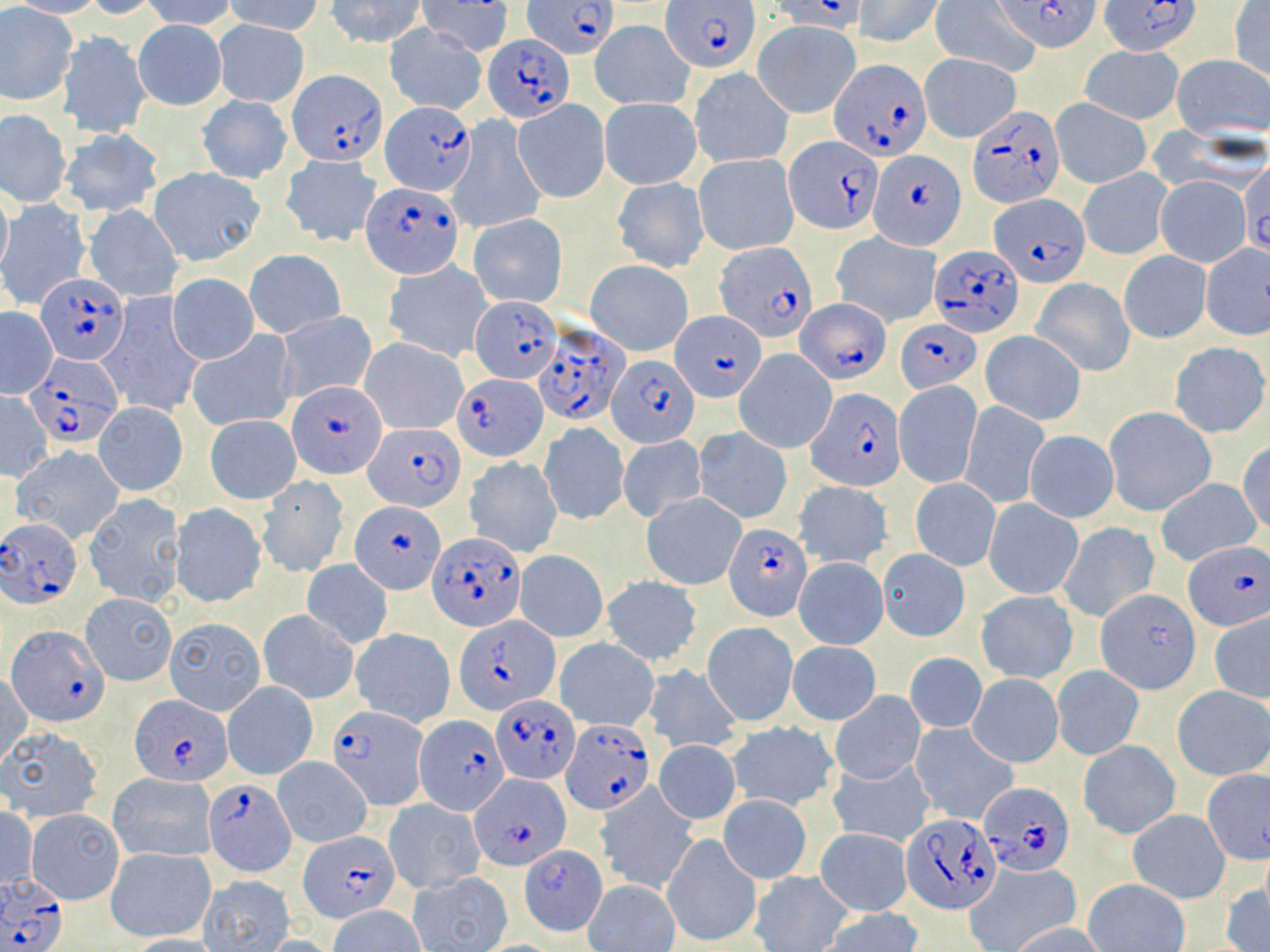 Approximate bounding boxes as (x1,y1)-(x2,y2) corner pairs in pixels. Plasmodium falciparum-infected red blood cell locations: (524,0)-(618,60), (663,0)-(758,72), (774,0)-(867,31), (994,1)-(1102,54), (1100,1)-(1204,55), (483,34)-(573,123), (831,57)-(933,169), (288,70)-(385,167), (379,101)-(475,193), (966,105)-(1065,208), (783,134)-(885,235), (869,150)-(964,251), (362,182)-(463,276), (990,196)-(1088,282), (715,241)-(817,340), (929,245)-(1023,337), (36,273)-(128,363), (469,296)-(565,385), (795,297)-(889,384), (673,312)-(763,401), (897,321)-(979,395), (534,322)-(629,428), (607,353)-(697,448), (26,355)-(122,445), (457,376)-(547,463), (288,379)-(386,477), (808,387)-(905,491), (365,422)-(465,511), (352,500)-(443,593), (1,517)-(83,609), (725,523)-(812,621), (427,532)-(527,631), (1183,540)-(1270,631), (1096,590)-(1199,693), (455,616)-(561,713), (7,625)-(108,725), (494,693)-(576,781), (131,696)-(230,786), (326,703)-(430,809), (414,714)-(509,815), (561,718)-(653,815), (471,774)-(570,870), (203,779)-(297,876), (980,781)-(1073,875), (900,814)-(1002,914), (299,830)-(399,924), (522,845)-(606,933), (0,873)-(69,952). Uninfected red blood cell locations: (7,0)-(107,18), (81,0)-(165,19), (141,0)-(239,31), (226,0)-(326,36), (325,0)-(426,48), (853,0)-(943,48), (927,0)-(1040,77), (419,1)-(513,54), (1229,3)-(1270,82), (0,6)-(78,107), (588,19)-(694,110), (753,19)-(861,118), (133,20)-(227,109), (213,20)-(309,107), (384,23)-(488,114), (58,32)-(149,138), (1079,45)-(1184,124), (919,53)-(1020,142), (1173,54)-(1270,139), (689,67)-(792,168), (197,95)-(293,184), (599,98)-(702,189), (1050,98)-(1152,189), (513,99)-(610,203), (0,112)-(71,206), (448,120)-(547,234), (61,132)-(163,217), (694,153)-(799,256), (280,155)-(383,247), (1239,164)-(1270,257), (150,167)-(265,264), (1078,167)-(1172,259), (1154,175)-(1251,267), (611,176)-(708,271), (0,187)-(13,282), (1,199)-(90,310), (86,204)-(184,301), (467,213)-(569,308), (829,232)-(941,328), (1201,244)-(1270,341), (245,249)-(345,337), (1118,250)-(1211,343), (383,260)-(492,362), (586,260)-(693,356), (167,273)-(259,364), (1031,277)-(1136,377), (97,296)-(205,418), (0,308)-(57,398), (275,310)-(378,404), (187,330)-(298,432), (980,330)-(1086,425), (360,336)-(468,434), (1168,341)-(1269,439), (734,350)-(837,454), (893,380)-(981,489), (0,391)-(53,480), (93,400)-(188,495), (959,400)-(1049,509), (1105,407)-(1216,517), (205,415)-(301,503), (538,422)-(629,525), (693,428)-(792,523), (1024,430)-(1118,522), (618,435)-(706,523), (1237,441)-(1270,538), (11,446)-(124,543), (465,457)-(563,558), (256,476)-(350,578), (1154,477)-(1261,566), (911,479)-(1000,572), (793,481)-(892,570), (641,492)-(747,589), (82,493)-(186,607), (983,498)-(1083,599), (169,502)-(266,608), (1057,523)-(1160,620), (880,549)-(971,642), (514,550)-(609,642), (793,557)-(887,648), (300,560)-(393,648), (602,576)-(702,667), (977,590)-(1077,683), (80,592)-(176,686), (258,609)-(360,703), (1209,610)-(1270,703), (165,614)-(266,714), (702,622)-(798,726), (350,627)-(456,727), (557,639)-(656,730), (787,642)-(881,724), (904,652)-(986,733), (642,664)-(743,753), (1052,665)-(1144,761), (1,671)-(32,767), (967,674)-(1063,768), (223,681)-(317,778), (1172,686)-(1270,780), (830,691)-(926,785), (728,720)-(840,811), (910,722)-(1017,825), (1,727)-(103,824), (1079,739)-(1178,839), (653,740)-(741,825), (273,756)-(372,847), (826,756)-(935,847), (108,772)-(217,863), (1192,775)-(1267,872), (595,784)-(697,895), (718,794)-(812,884), (384,798)-(485,893), (0,807)-(37,893), (28,809)-(122,902), (1128,810)-(1230,902), (814,828)-(913,916), (663,833)-(760,946), (105,846)-(215,942), (962,860)-(1081,952), (750,871)-(853,952), (407,873)-(512,952), (200,875)-(295,950), (1084,879)-(1190,952), (582,880)-(680,952), (1220,883)-(1270,952), (328,905)-(424,951), (819,907)-(923,952), (1005,922)-(1108,952), (122,934)-(224,952), (257,936)-(338,951). Slide-level diagnosis: Plasmodium falciparum. One field of a larger specimen. Light microscopy. Captured at 1000x magnification. May-Grünwald-Giemsa-stained preparation. Image is 1270×952 pixels. Thin blood film.